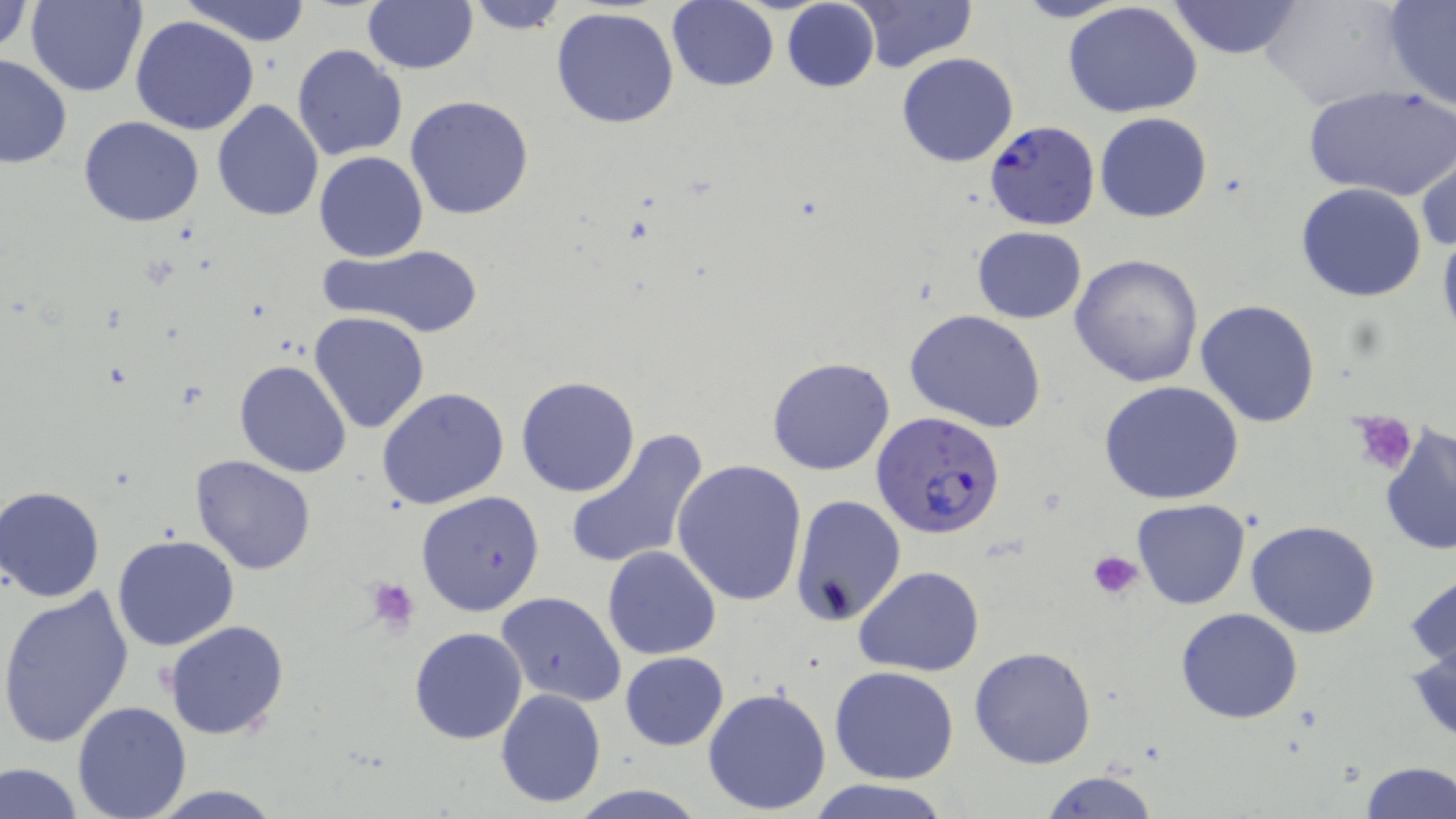
Approximate bounding boxes as (x1, y1, x2, y2) in pixels. Platelet locations: (1348, 410, 1418, 477), (1087, 550, 1143, 599), (367, 578, 421, 632). Plasmodium falciparum-infected red blood cell locations: (984, 122, 1100, 232), (871, 411, 1007, 541). Uninfected red blood cell locations: (25, 0, 148, 98), (182, 0, 314, 46), (362, 0, 477, 73), (1010, 0, 1133, 23), (1061, 0, 1203, 120), (1167, 0, 1303, 58), (1261, 0, 1409, 110), (1381, 0, 1456, 113), (1, 1, 34, 59), (461, 1, 572, 35), (667, 1, 779, 91), (781, 1, 879, 94), (848, 1, 979, 73), (550, 8, 680, 129), (130, 16, 258, 135), (291, 44, 409, 163), (897, 52, 1018, 167), (0, 53, 72, 168), (1303, 84, 1456, 203), (404, 95, 535, 221), (211, 100, 324, 221), (1095, 113, 1213, 223), (78, 116, 205, 227), (1416, 149, 1455, 257), (314, 151, 427, 261), (1297, 183, 1427, 302), (1436, 223, 1456, 345), (972, 226, 1087, 322), (318, 243, 485, 339), (1070, 254, 1205, 389), (1196, 299, 1322, 428), (904, 309, 1047, 432), (308, 311, 430, 435), (767, 355, 896, 476), (234, 360, 351, 477), (515, 376, 641, 498), (1099, 379, 1247, 504), (377, 387, 510, 511), (1380, 424, 1456, 556), (563, 428, 709, 573), (189, 455, 317, 575), (673, 458, 807, 606), (1, 487, 106, 601), (415, 490, 546, 616), (790, 494, 907, 627), (1132, 499, 1250, 609), (1247, 520, 1381, 638), (112, 535, 239, 652), (602, 545, 721, 661), (854, 564, 986, 676), (1406, 565, 1456, 673), (0, 589, 135, 747), (497, 592, 625, 708), (1176, 606, 1303, 723), (164, 619, 290, 739), (1408, 623, 1456, 745), (409, 627, 528, 744), (969, 645, 1095, 769), (620, 651, 729, 750), (830, 665, 960, 784), (703, 686, 832, 815), (496, 688, 606, 808), (71, 701, 192, 818), (0, 759, 84, 819), (1358, 762, 1455, 819), (1039, 771, 1162, 818), (808, 778, 952, 819), (564, 785, 712, 818). Slide-level diagnosis: Plasmodium falciparum. Light microscopy. Single field of view. Image is 1456×819 pixels. May-Grünwald-Giemsa-stained preparation. Thin blood smear. Captured at 1000x magnification.